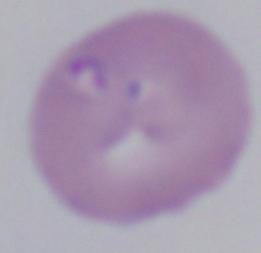
Photomicrograph. A Babesia parasite is shown. 1000x magnification.